Classify this cell by malaria status.
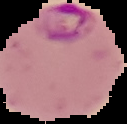
It is parasitized.

image size = 127×124 pixels
preparation = thin blood smear
image type = cell region segmented out of the field of view; surrounding area masked to black